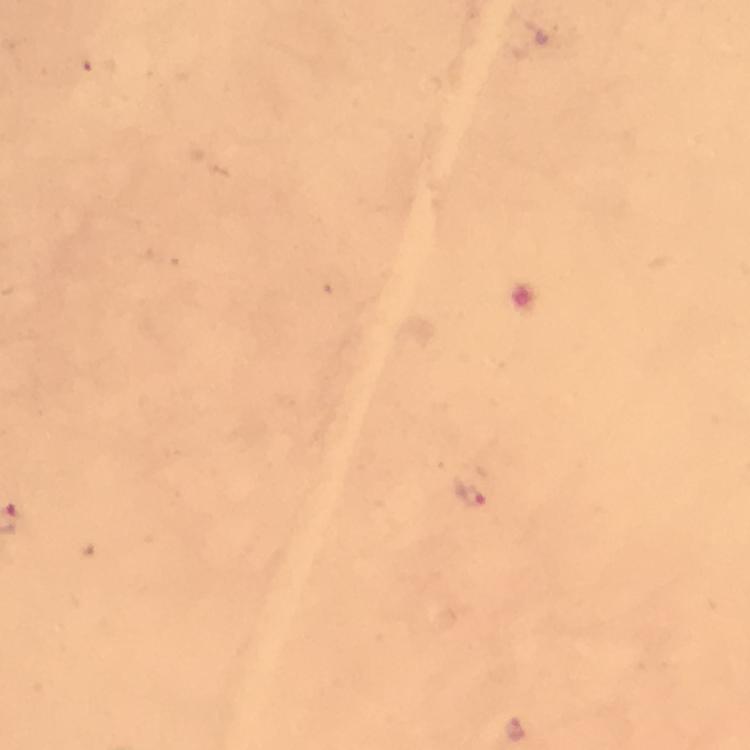

Approximate centers as (x, y) in pixels.
Summary:
  - Malaria parasite locations: (470, 495), (515, 728)
  - Magnification: 100x
  - Immersion oil: used
  - Preparation: thick smear
  - Stain: Giemsa
  - Capture: smartphone mounted on the microscope
  - Cropped from: a single field of view
  - Context: from a malaria diagnostic workup
  - Image size: 750×750 pixels